Classify this cell by malaria status.
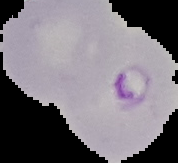
It is parasitized.

The area outside the segmented cell region is set to black. Image is 178×163 pixels. From a thin blood film.